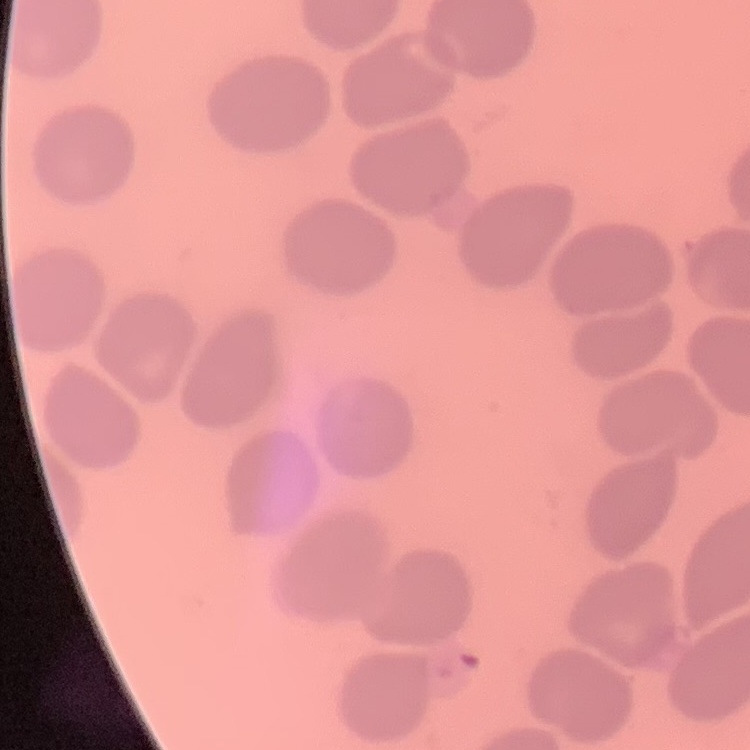
Summary:
  - Red blood cell morphology: no rouleaux formation
  - Image type: one tile cut from a larger photomicrograph
  - Stain: Field's or Giemsa
  - Preparation: thin blood film